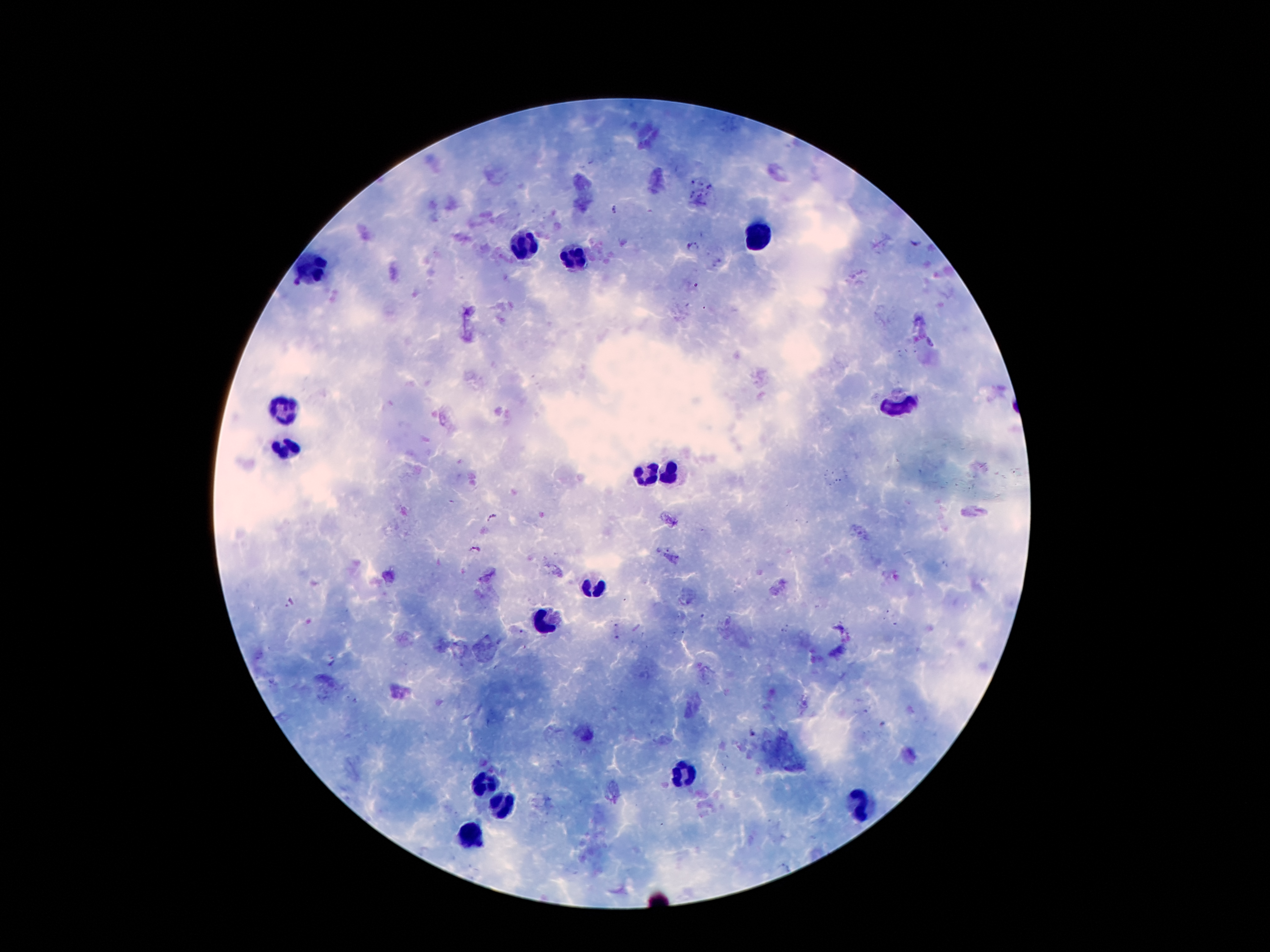 Approximate object centers, in pixels from the top-left corner. Malaria parasite locations: (x=616, y=208), (x=915, y=243), (x=691, y=245), (x=491, y=518), (x=474, y=549), (x=290, y=602). Leukocyte locations: (x=755, y=234), (x=522, y=247), (x=574, y=260), (x=316, y=270), (x=895, y=408), (x=284, y=410), (x=286, y=451), (x=670, y=473), (x=648, y=476), (x=594, y=588), (x=550, y=624), (x=685, y=775), (x=487, y=784), (x=497, y=802), (x=863, y=803), (x=469, y=836). Patient malaria status: infected with Plasmodium falciparum. Image is 1270×952 pixels. Photographed through the microscope eyepiece with a smartphone camera. Single field of view. 100x magnification. Thick blood film. Giemsa-stained preparation.